Identify the preparation type.
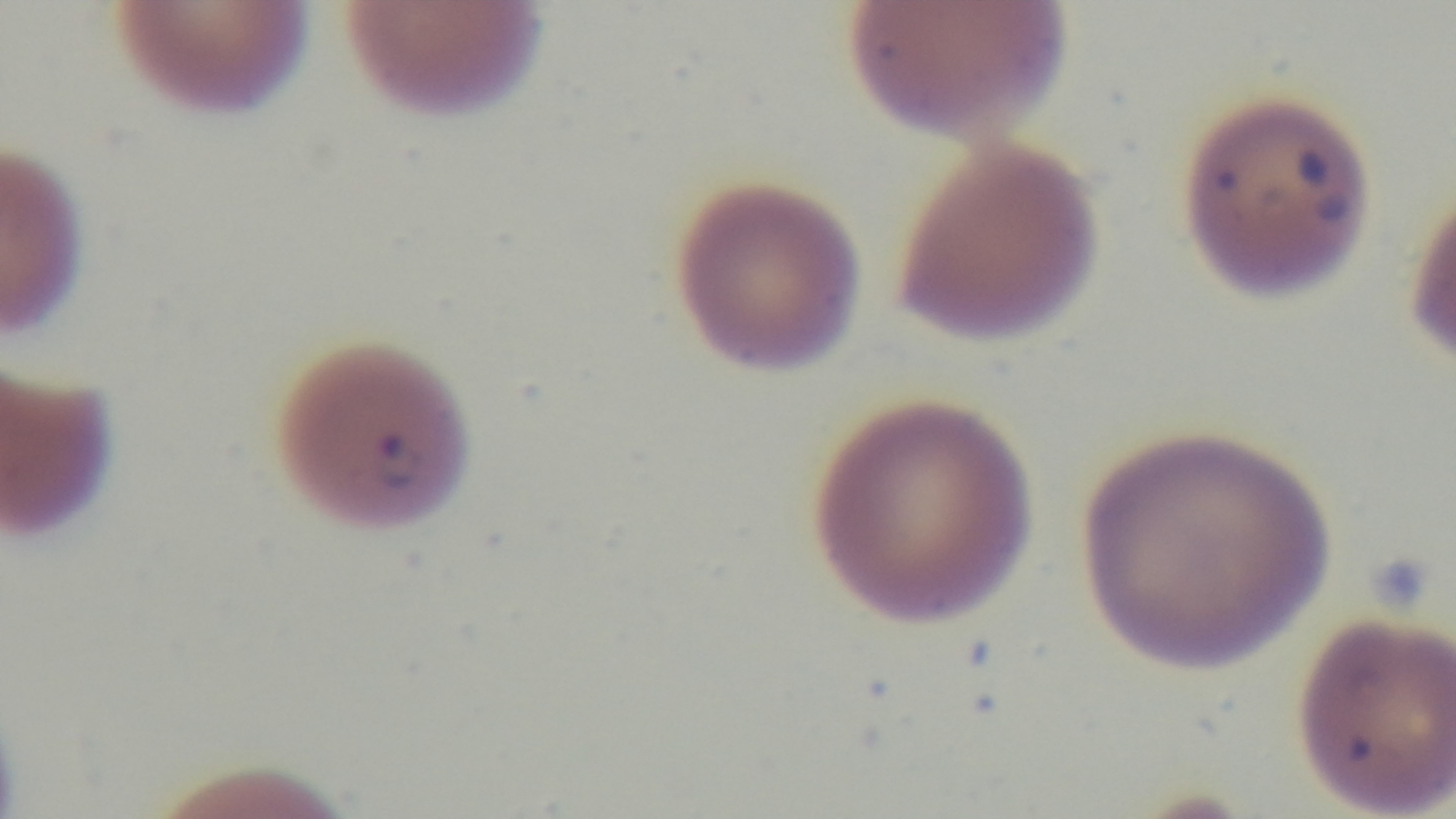

It is a thin blood film.

modality = light microscopy
field of view = one from the slide
capture = mounted 4K digital camera
objective = 100x oil immersion
malaria status = infected
stain = Giemsa